Identify the parasite.
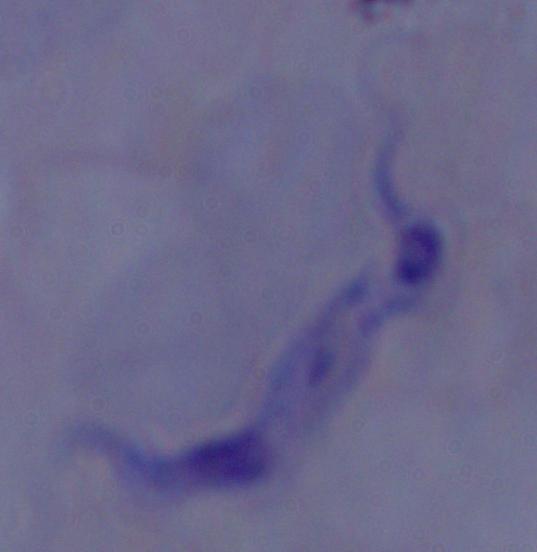

A trypanosome.

magnification = 1000x
modality = micrograph